Give the position of every Plasmodium parasite, noting whether each is a trophozoite, schizont, or gametocyte.
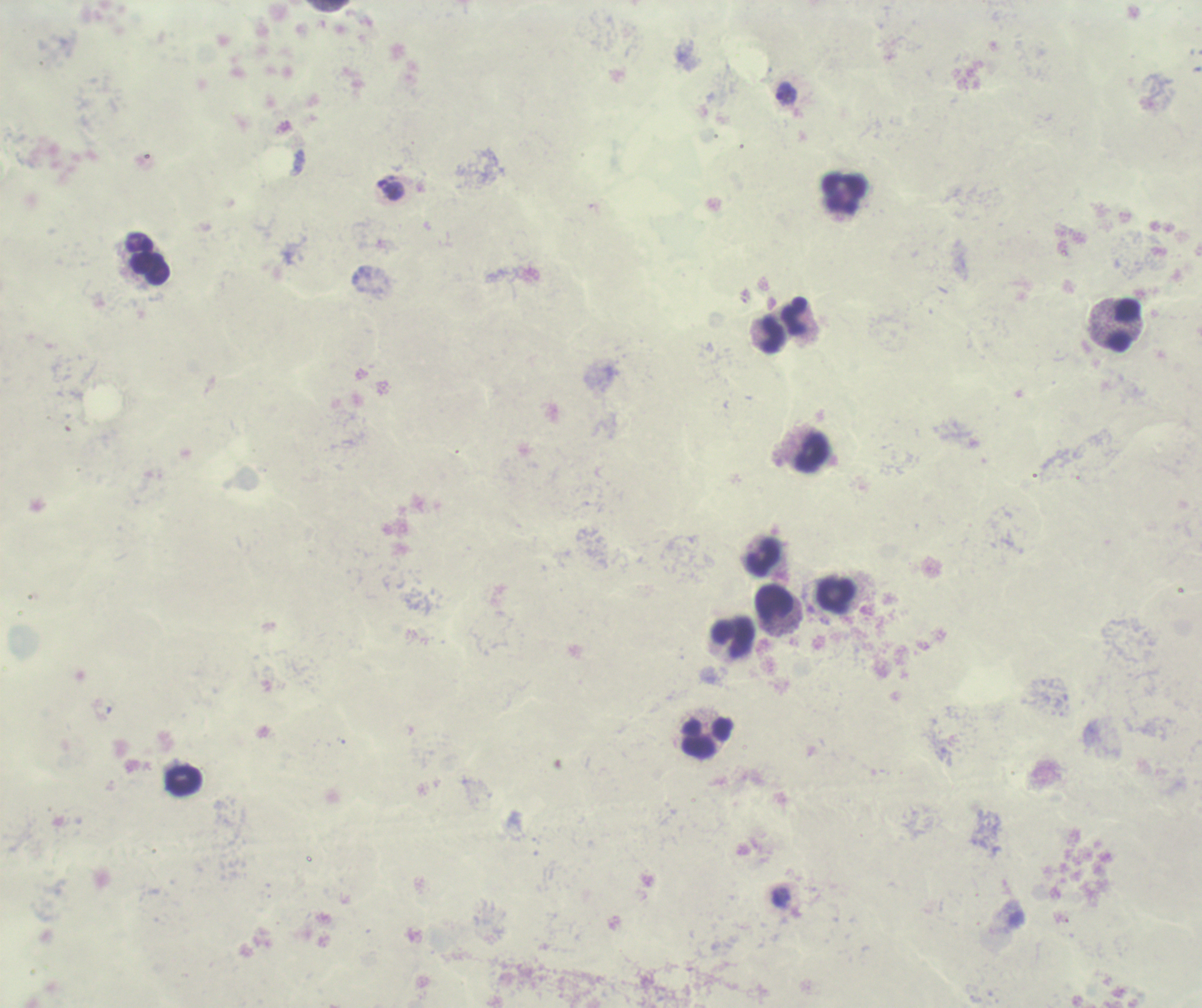

Approximate centers as (x, y) in pixels.
Trophozoites: (787, 94), (390, 189), (781, 897).
No schizont or gametocyte forms observed.

Approximate centers as (x, y) in pixels.
Summary:
  - Leukocyte locations: (844, 194), (150, 268), (794, 316), (1124, 325), (773, 335), (810, 451), (763, 557), (835, 595), (774, 602), (733, 637), (708, 738), (183, 781)
  - Field of view: one from this slide
  - Preparation: thick smear of blood
  - Background quality: poor
  - Image size: 1202×1008 pixels
  - Context: previously used in an actual diagnosis
  - Coloration quality: bad
  - Stain: Romanowsky
  - Magnification: 100x